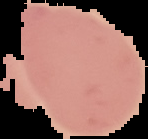 Malaria status: uninfected. From a thin blood smear. Image is 148×139 pixels. Segmented cell region on a black background.